State which cell type is depicted.
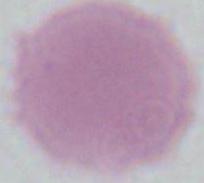
An erythrocyte.

Captured at 1000x magnification. Photomicrograph.